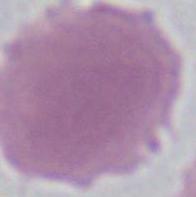
Captured at 1000x magnification. Micrograph. A red blood cell is shown.